Identify the blood parasite species.
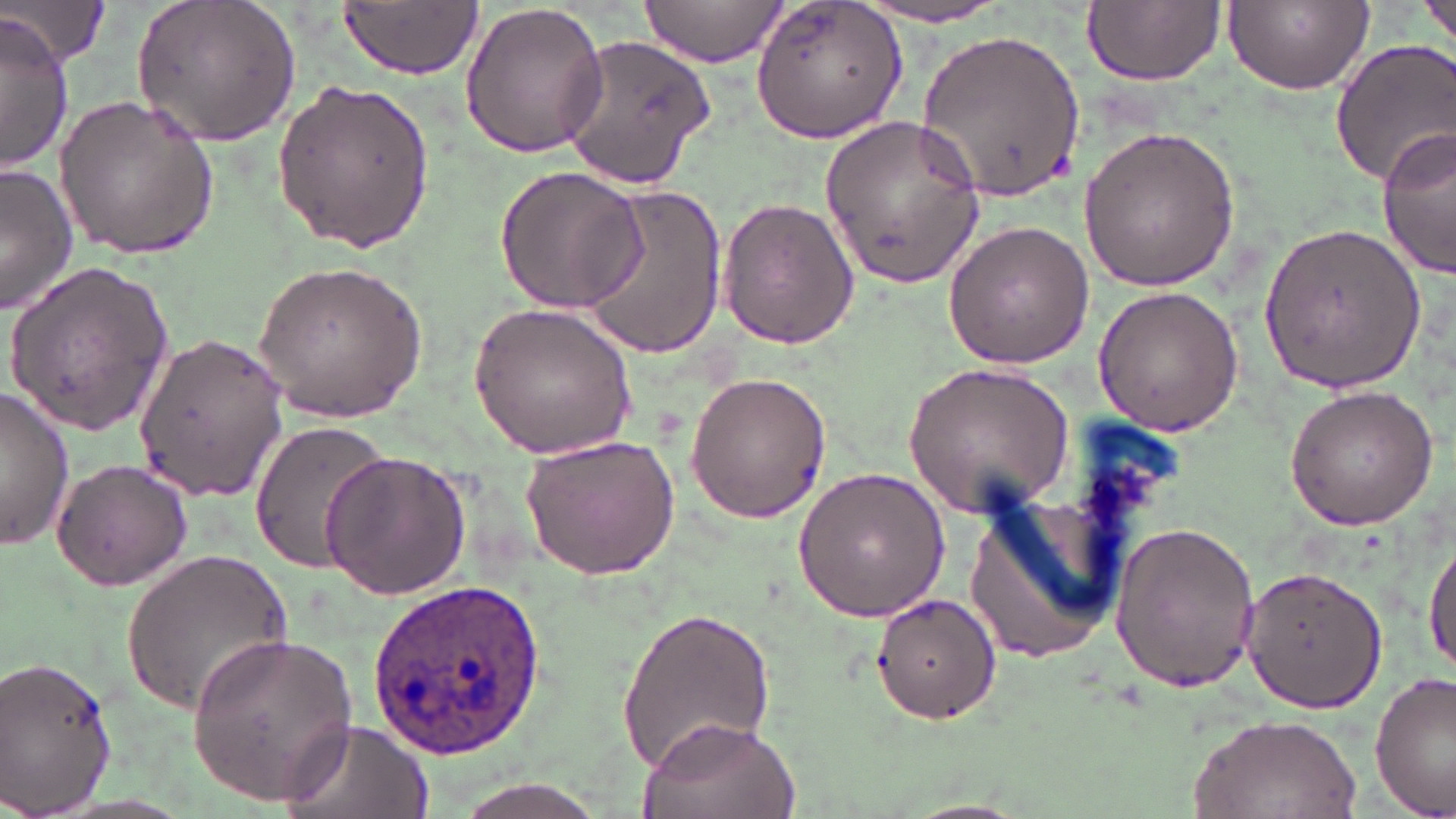
Plasmodium ovale.

Summary:
  - Coordinate format: approximate bounding boxes as named x1/y1/x2/y2 corners in pixels
  - Uninfected red blood cell locations: (x1=3, y1=0, x2=111, y2=70), (x1=133, y1=0, x2=301, y2=149), (x1=638, y1=0, x2=787, y2=68), (x1=1222, y1=0, x2=1375, y2=93), (x1=1418, y1=0, x2=1454, y2=52), (x1=337, y1=1, x2=483, y2=79), (x1=749, y1=1, x2=909, y2=146), (x1=1083, y1=1, x2=1225, y2=86), (x1=850, y1=3, x2=1022, y2=28), (x1=458, y1=4, x2=610, y2=160), (x1=0, y1=18, x2=75, y2=173), (x1=922, y1=26, x2=1086, y2=201), (x1=559, y1=33, x2=719, y2=190), (x1=1328, y1=37, x2=1456, y2=187), (x1=270, y1=79, x2=439, y2=254), (x1=53, y1=95, x2=222, y2=260), (x1=819, y1=113, x2=986, y2=289), (x1=1076, y1=124, x2=1241, y2=294), (x1=1377, y1=130, x2=1455, y2=278), (x1=0, y1=163, x2=78, y2=313), (x1=493, y1=164, x2=648, y2=314), (x1=572, y1=180, x2=727, y2=358), (x1=717, y1=195, x2=859, y2=349), (x1=1255, y1=217, x2=1427, y2=393), (x1=941, y1=218, x2=1096, y2=369), (x1=252, y1=258, x2=428, y2=421), (x1=5, y1=261, x2=173, y2=438), (x1=1092, y1=284, x2=1245, y2=439), (x1=468, y1=301, x2=639, y2=458), (x1=132, y1=332, x2=288, y2=502), (x1=903, y1=358, x2=1078, y2=517), (x1=684, y1=370, x2=832, y2=525), (x1=1283, y1=384, x2=1439, y2=530), (x1=0, y1=388, x2=75, y2=550), (x1=246, y1=420, x2=394, y2=575), (x1=519, y1=436, x2=680, y2=580), (x1=320, y1=449, x2=470, y2=600), (x1=50, y1=458, x2=193, y2=590), (x1=791, y1=466, x2=955, y2=621), (x1=963, y1=494, x2=1128, y2=665), (x1=1108, y1=521, x2=1262, y2=693), (x1=1424, y1=533, x2=1456, y2=676), (x1=121, y1=548, x2=294, y2=714), (x1=1240, y1=565, x2=1388, y2=712), (x1=872, y1=591, x2=1003, y2=724), (x1=615, y1=602, x2=775, y2=777), (x1=186, y1=631, x2=360, y2=805), (x1=0, y1=654, x2=119, y2=818), (x1=1370, y1=674, x2=1454, y2=815), (x1=1190, y1=713, x2=1363, y2=817), (x1=639, y1=714, x2=803, y2=819), (x1=279, y1=716, x2=434, y2=819), (x1=447, y1=780, x2=613, y2=819)
  - Plasmodium ovale-infected red blood cell locations: (x1=367, y1=575, x2=553, y2=758)
  - Image size: 1456×819 pixels
  - Stain: May-Grünwald-Giemsa
  - Magnification: 1000x
  - Preparation: thin blood smear
  - Modality: light microscopy
  - Field of view: single